Identify the preparation type.
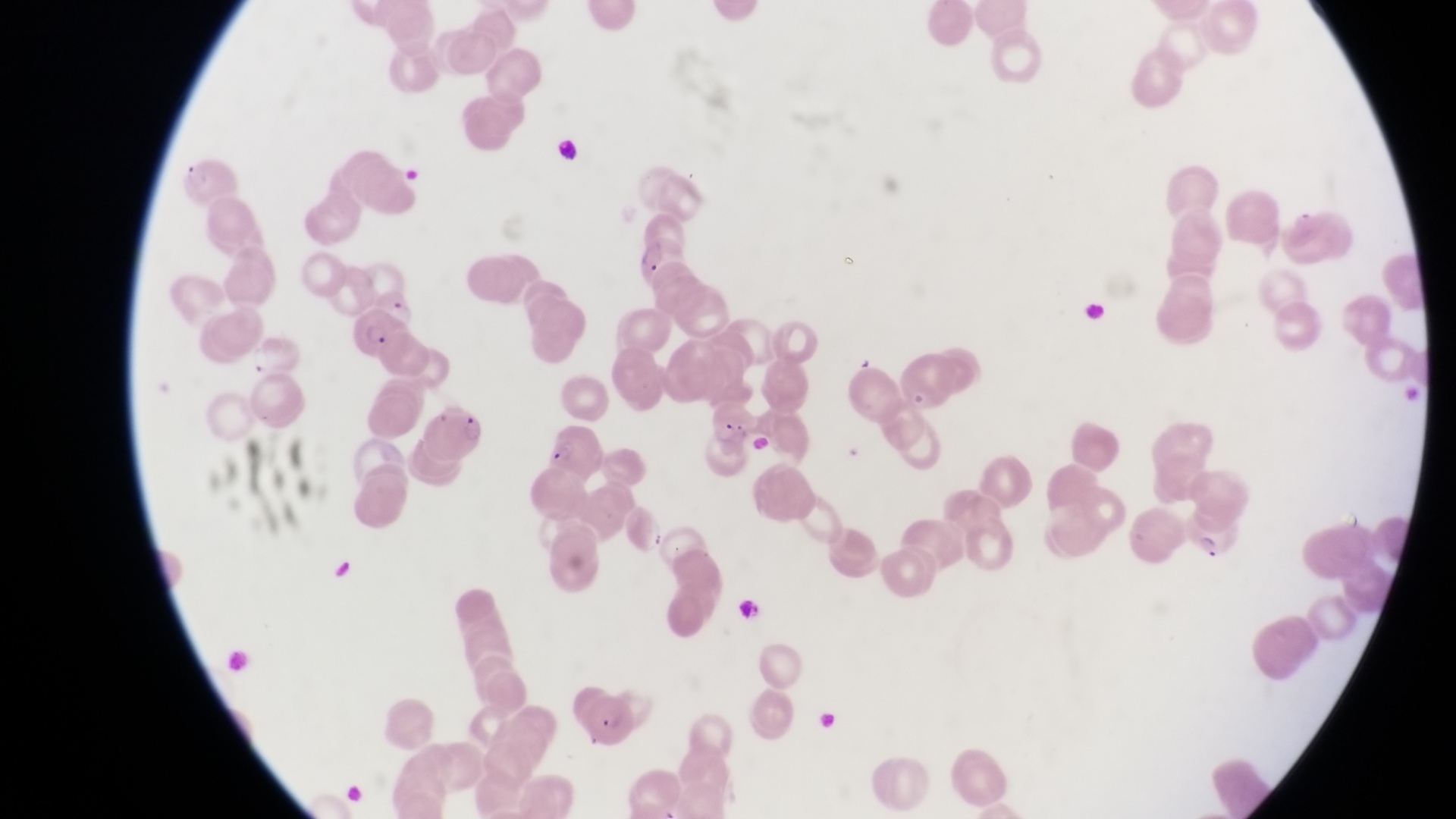
Thin blood film.

magnification = 1000x
image size = 1456×819 pixels
country = Uganda
field of view = single
parasitised red blood cell locations = approximate bounding boxes as [left, top, right, bottom] in pixels: [179, 162, 239, 204], [635, 238, 691, 284], [351, 309, 412, 364], [706, 399, 761, 448], [425, 403, 484, 463], [542, 425, 602, 481], [1182, 504, 1241, 568], [582, 693, 641, 751]
capture = smartphone photograph through the eyepiece of an Olympus CX-23 microscope
artifact (platelet-like body, stain precipitate, or debris) locations = approximate bounding boxes as [left, top, right, bottom] in pixels: [732, 592, 758, 618]